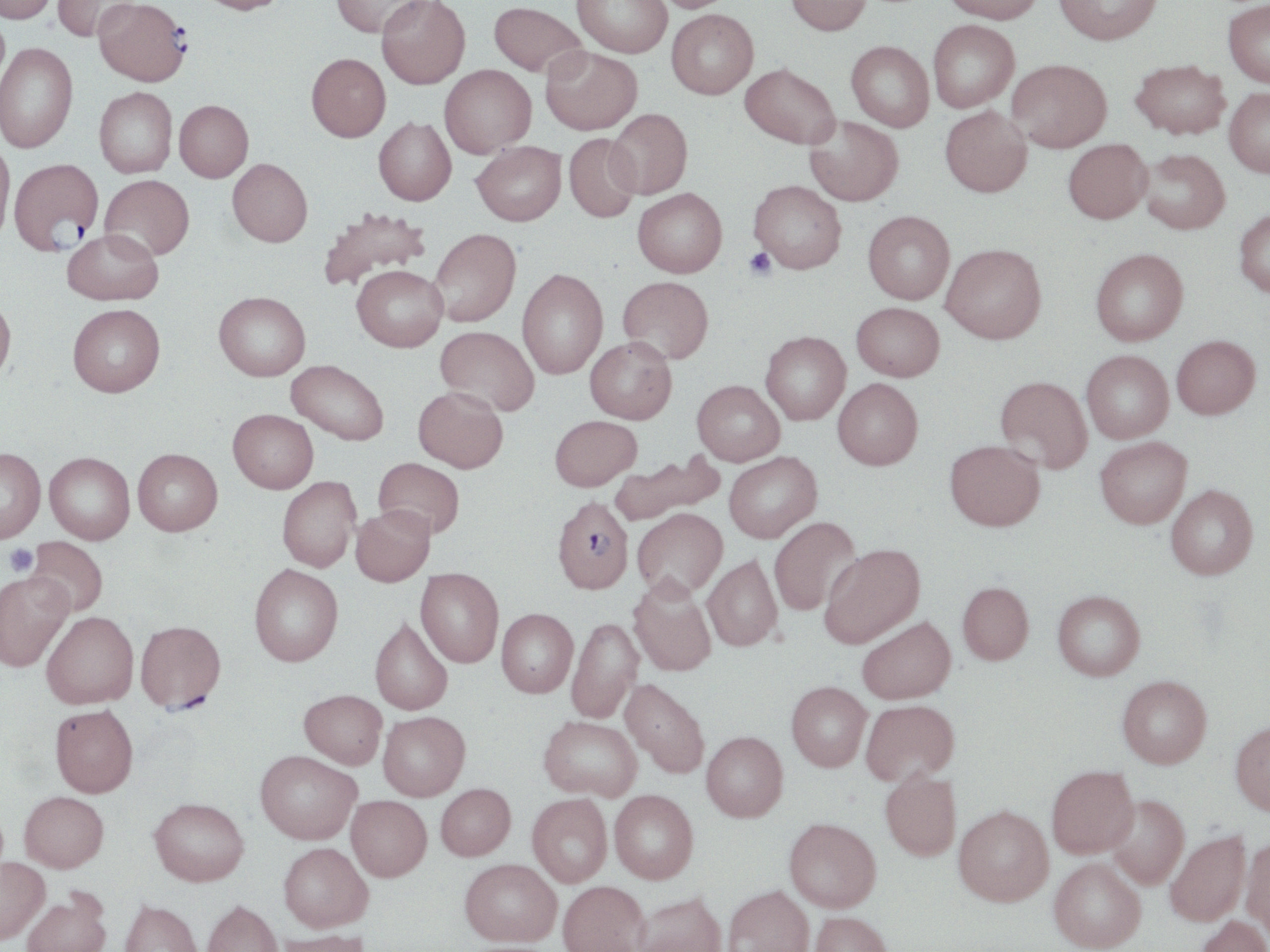

{
  "plasmodium_falciparum_infected_red_blood_cell_locations": "approximate bounding boxes as (x1, y1, x2, y2) in pixels: (94, 0, 191, 87), (8, 158, 103, 255), (551, 495, 634, 594), (135, 620, 226, 714)",
  "slide_level_diagnosis": "Plasmodium falciparum",
  "preparation": "thin blood smear",
  "image_size": "1270×952 pixels",
  "uninfected_red_blood_cell_locations": "approximate bounding boxes as (x1, y1, x2, y2) in pixels: (0, 0, 56, 23), (52, 0, 138, 42), (196, 0, 292, 14), (331, 0, 431, 38), (376, 0, 470, 88), (572, 0, 672, 57), (647, 0, 735, 12), (786, 0, 872, 35), (942, 0, 1045, 23), (1054, 0, 1163, 44), (489, 1, 587, 77), (1222, 1, 1270, 87), (666, 9, 758, 98), (927, 20, 1019, 113), (846, 41, 934, 132), (0, 43, 78, 152), (541, 46, 642, 135), (306, 53, 391, 142), (1007, 59, 1112, 151), (1130, 59, 1230, 139), (740, 63, 840, 148), (440, 64, 536, 157), (94, 87, 178, 177), (1224, 88, 1270, 177), (174, 100, 253, 182), (940, 106, 1033, 197), (607, 108, 693, 199), (373, 117, 456, 205), (804, 117, 904, 206), (563, 134, 642, 222), (1063, 139, 1152, 223), (0, 141, 14, 244), (472, 142, 566, 226), (1139, 149, 1230, 234), (227, 158, 313, 246), (100, 174, 194, 261), (749, 180, 847, 273), (633, 188, 727, 277), (316, 207, 431, 292), (1234, 208, 1270, 298), (863, 211, 955, 304), (430, 228, 521, 326), (62, 229, 163, 305), (941, 244, 1046, 344), (1090, 248, 1188, 345), (352, 265, 447, 351), (517, 268, 607, 379), (618, 276, 714, 363), (213, 291, 310, 380), (0, 295, 16, 383), (852, 302, 944, 382), (67, 304, 165, 397), (434, 326, 539, 416), (760, 331, 851, 424), (1172, 335, 1260, 419), (585, 337, 677, 423), (1081, 351, 1173, 443), (286, 359, 389, 446), (995, 376, 1093, 473), (833, 378, 923, 469), (692, 380, 785, 465), (413, 386, 508, 472), (228, 409, 318, 493), (550, 415, 641, 490), (1095, 437, 1191, 528), (945, 439, 1045, 531), (0, 447, 45, 542), (133, 448, 222, 535), (723, 451, 822, 543), (45, 452, 135, 544), (610, 452, 724, 526), (373, 457, 465, 539), (277, 476, 360, 572), (1166, 484, 1258, 579), (351, 505, 435, 586), (632, 508, 727, 599), (769, 516, 862, 615), (25, 536, 108, 617), (819, 544, 925, 648), (703, 554, 782, 651), (248, 564, 344, 666), (415, 567, 504, 667), (0, 570, 73, 671), (628, 576, 717, 676), (957, 581, 1034, 665), (1053, 590, 1145, 680), (496, 608, 577, 697), (41, 611, 138, 708), (370, 616, 453, 715), (566, 616, 643, 723), (857, 616, 955, 703), (1117, 675, 1212, 767), (620, 678, 710, 778), (787, 681, 872, 771), (299, 689, 387, 768), (860, 699, 959, 786), (50, 704, 139, 797), (378, 711, 470, 800), (538, 715, 641, 801), (1230, 721, 1270, 815), (701, 731, 787, 821), (255, 750, 361, 844), (1047, 765, 1138, 857), (880, 768, 960, 860), (435, 783, 515, 860), (609, 790, 698, 883), (19, 791, 109, 872), (527, 794, 612, 887), (346, 795, 431, 881), (1107, 795, 1189, 889), (149, 797, 248, 886), (954, 805, 1053, 905), (784, 817, 881, 911), (1165, 830, 1250, 926), (1241, 836, 1270, 941), (279, 842, 373, 932), (0, 856, 49, 943), (1049, 858, 1146, 951), (459, 859, 560, 946), (558, 880, 649, 952), (723, 885, 814, 952), (21, 888, 111, 952), (631, 891, 727, 952), (119, 899, 203, 952), (202, 899, 283, 952), (809, 911, 894, 952), (1195, 915, 1270, 952), (272, 929, 372, 952)",
  "field_of_view": "one of a larger specimen",
  "stain": "May-Grünwald-Giemsa",
  "platelet_locations": "approximate bounding boxes as (x1, y1, x2, y2) in pixels: (744, 248, 776, 279), (4, 544, 38, 576)",
  "modality": "light microscopy",
  "magnification": "1000x"
}